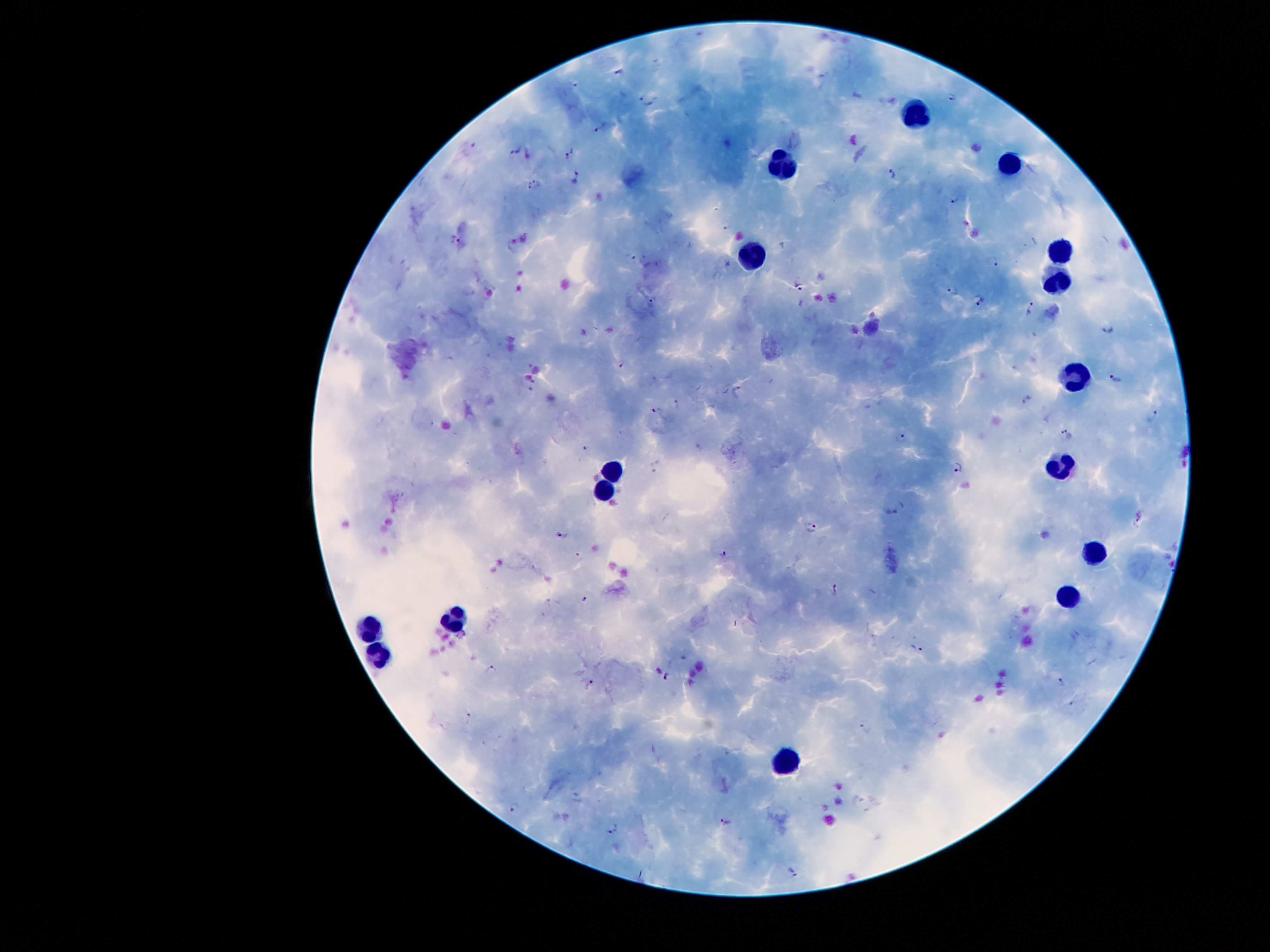 Approximate centers as [x, y] in pixels. Leukocyte locations: [913, 119], [788, 164], [1006, 165], [1060, 252], [750, 256], [1054, 282], [1076, 375], [1059, 464], [614, 469], [603, 493], [1097, 543], [1065, 600], [455, 624], [371, 626], [379, 652], [787, 768]. Plasmodium parasite locations: [642, 96], [953, 97], [654, 103], [601, 128], [517, 151], [571, 155], [893, 175], [577, 178], [535, 184], [955, 198], [455, 241], [630, 256], [993, 262], [798, 286], [952, 291], [654, 299], [979, 300], [1032, 307], [1106, 328], [621, 364], [1116, 380], [737, 391], [1028, 399], [656, 411], [1154, 418], [1066, 435], [899, 437], [587, 448], [959, 466], [890, 512], [1140, 517], [811, 528], [563, 534], [723, 552], [837, 589], [586, 599], [919, 648], [491, 670], [666, 677], [1063, 678], [591, 684], [469, 716], [867, 726], [515, 806], [725, 822], [613, 828], [795, 873]. Patient malaria status: infected with Plasmodium falciparum. Smartphone photograph taken through the microscope eyepiece. 100x magnification. Thick blood smear. Image is 1270×952 pixels. Giemsa-stained preparation. Single field of view.